Locate and identify every blood parasite.
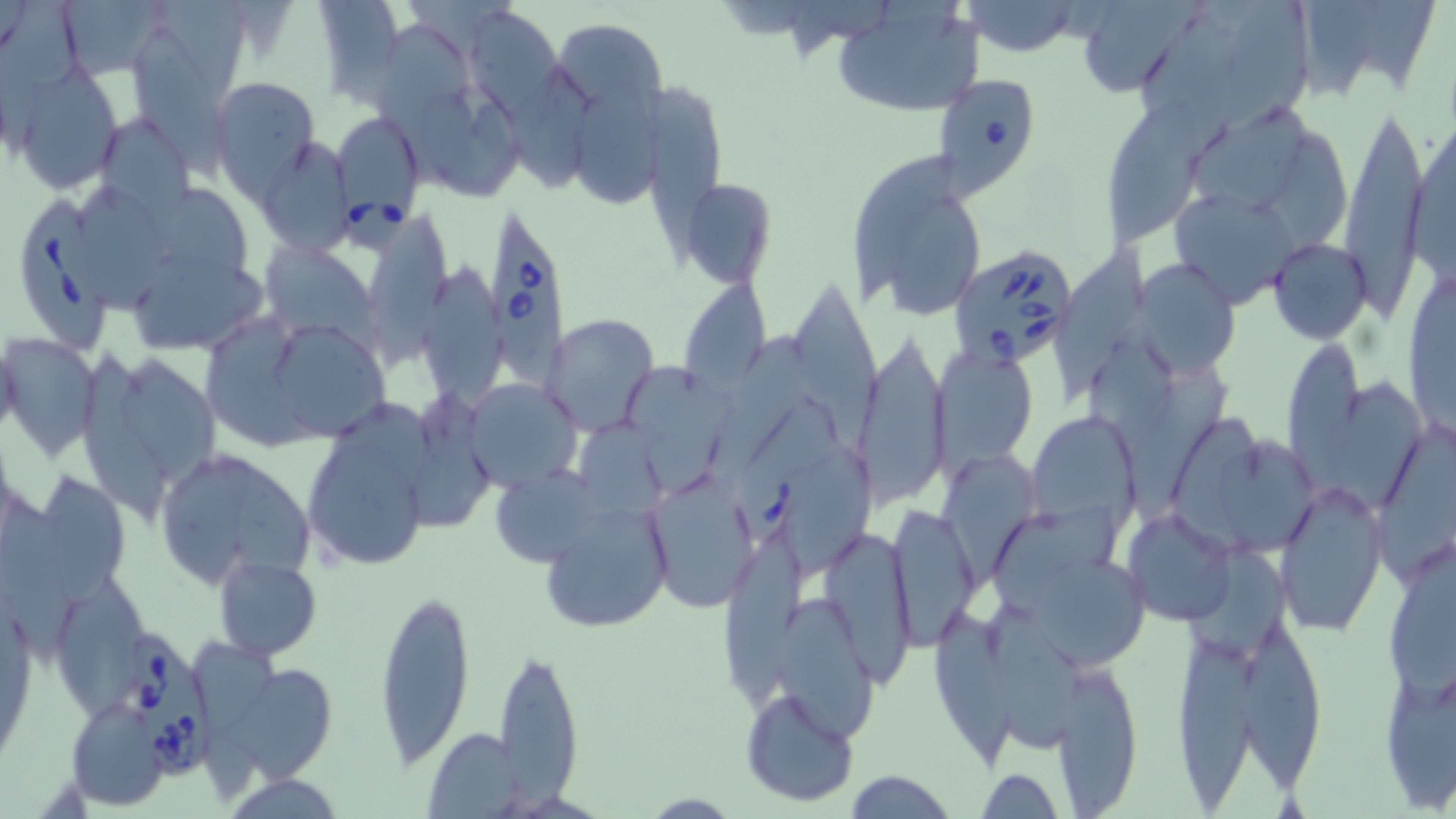

Approximate bounding boxes as named x1/y1/x2/y2 corners in pixels.
Babesia divergens-infected red blood cells: (x1=932, y1=74, x2=1045, y2=201), (x1=338, y1=120, x2=421, y2=255), (x1=23, y1=199, x2=110, y2=352), (x1=487, y1=213, x2=568, y2=391), (x1=949, y1=242, x2=1081, y2=371), (x1=742, y1=397, x2=845, y2=546), (x1=127, y1=633, x2=215, y2=778).
No Plasmodium falciparum, Plasmodium ovale, Plasmodium malariae, Plasmodium vivax, or Trypanosoma brucei observed.

slide-level diagnosis = Babesia divergens
uninfected red blood cell locations = approximate bounding boxes as named x1/y1/x2/y2 corners in pixels: (x1=313, y1=0, x2=401, y2=104), (x1=1075, y1=0, x2=1204, y2=100), (x1=1225, y1=0, x2=1310, y2=132), (x1=1359, y1=0, x2=1436, y2=89), (x1=57, y1=1, x2=177, y2=80), (x1=831, y1=1, x2=985, y2=119), (x1=961, y1=2, x2=1081, y2=56), (x1=1301, y1=3, x2=1376, y2=101), (x1=167, y1=4, x2=249, y2=93), (x1=470, y1=11, x2=562, y2=118), (x1=1140, y1=11, x2=1239, y2=113), (x1=378, y1=23, x2=468, y2=169), (x1=559, y1=26, x2=669, y2=117), (x1=136, y1=29, x2=232, y2=194), (x1=11, y1=67, x2=124, y2=193), (x1=511, y1=69, x2=597, y2=200), (x1=209, y1=77, x2=320, y2=198), (x1=649, y1=84, x2=729, y2=273), (x1=425, y1=90, x2=521, y2=200), (x1=573, y1=92, x2=660, y2=210), (x1=1338, y1=95, x2=1429, y2=317), (x1=1106, y1=96, x2=1205, y2=249), (x1=1190, y1=106, x2=1307, y2=217), (x1=1406, y1=110, x2=1456, y2=293), (x1=103, y1=114, x2=195, y2=253), (x1=1264, y1=131, x2=1347, y2=257), (x1=257, y1=139, x2=360, y2=259), (x1=850, y1=152, x2=958, y2=301), (x1=681, y1=179, x2=776, y2=286), (x1=153, y1=181, x2=252, y2=290), (x1=80, y1=183, x2=174, y2=313), (x1=1168, y1=194, x2=1297, y2=310), (x1=894, y1=198, x2=979, y2=317), (x1=372, y1=215, x2=448, y2=380), (x1=1268, y1=238, x2=1373, y2=343), (x1=268, y1=242, x2=386, y2=359), (x1=1056, y1=243, x2=1148, y2=400), (x1=124, y1=246, x2=274, y2=351), (x1=1132, y1=256, x2=1240, y2=375), (x1=423, y1=267, x2=504, y2=413), (x1=679, y1=277, x2=769, y2=397), (x1=796, y1=282, x2=879, y2=457), (x1=543, y1=313, x2=658, y2=434), (x1=209, y1=316, x2=320, y2=446), (x1=278, y1=328, x2=387, y2=439), (x1=852, y1=330, x2=950, y2=504), (x1=710, y1=331, x2=816, y2=486), (x1=1, y1=333, x2=105, y2=462), (x1=1281, y1=337, x2=1367, y2=495), (x1=1094, y1=340, x2=1182, y2=455), (x1=935, y1=346, x2=1038, y2=471), (x1=85, y1=353, x2=171, y2=526), (x1=122, y1=356, x2=216, y2=479), (x1=631, y1=365, x2=735, y2=494), (x1=1130, y1=370, x2=1230, y2=518), (x1=1331, y1=378, x2=1430, y2=511), (x1=463, y1=381, x2=584, y2=488), (x1=414, y1=382, x2=495, y2=537), (x1=344, y1=399, x2=434, y2=491), (x1=1026, y1=410, x2=1139, y2=533), (x1=1172, y1=410, x2=1265, y2=538), (x1=579, y1=420, x2=675, y2=516), (x1=1377, y1=424, x2=1456, y2=582), (x1=297, y1=437, x2=433, y2=562), (x1=1224, y1=438, x2=1314, y2=556), (x1=783, y1=443, x2=877, y2=578), (x1=945, y1=451, x2=1034, y2=583), (x1=223, y1=458, x2=316, y2=578), (x1=497, y1=463, x2=608, y2=564), (x1=163, y1=466, x2=251, y2=587), (x1=42, y1=472, x2=128, y2=608), (x1=644, y1=473, x2=757, y2=612), (x1=1276, y1=477, x2=1390, y2=639), (x1=0, y1=490, x2=83, y2=666), (x1=537, y1=501, x2=672, y2=634), (x1=885, y1=506, x2=980, y2=648), (x1=1123, y1=509, x2=1238, y2=628), (x1=997, y1=511, x2=1117, y2=611), (x1=725, y1=531, x2=809, y2=716), (x1=830, y1=536, x2=913, y2=691), (x1=1185, y1=545, x2=1297, y2=664), (x1=1027, y1=551, x2=1152, y2=669), (x1=1388, y1=553, x2=1456, y2=709), (x1=215, y1=556, x2=322, y2=660), (x1=61, y1=576, x2=149, y2=722), (x1=373, y1=587, x2=476, y2=768), (x1=780, y1=598, x2=879, y2=750), (x1=978, y1=603, x2=1086, y2=749), (x1=934, y1=609, x2=1015, y2=770), (x1=1243, y1=629, x2=1324, y2=797), (x1=1172, y1=630, x2=1257, y2=811), (x1=193, y1=641, x2=280, y2=795), (x1=493, y1=644, x2=584, y2=807), (x1=214, y1=659, x2=339, y2=784), (x1=1378, y1=661, x2=1456, y2=811), (x1=1054, y1=664, x2=1142, y2=813), (x1=740, y1=687, x2=859, y2=807), (x1=67, y1=697, x2=169, y2=808), (x1=423, y1=728, x2=525, y2=816), (x1=976, y1=767, x2=1062, y2=819), (x1=842, y1=769, x2=955, y2=818)
preparation = thin blood film
image size = 1456×819 pixels
stain = May-Grünwald-Giemsa
magnification = 1000x
modality = light microscopy
field of view = one of a larger specimen